Assess this cell for malaria.
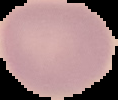
It is uninfected.

preparation = thin blood smear
image type = cell region segmented out of the field of view; surrounding area masked to black
image size = 118×100 pixels